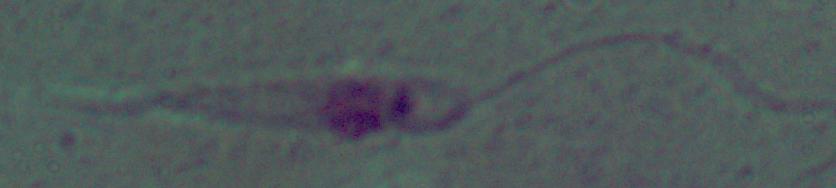
Photomicrograph. Captured at 1000x magnification. A Leishmania parasite is shown.